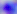
Toxoplasma gondii is seen. Photomicrograph. Captured at 400x magnification.